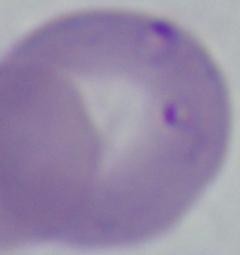

magnification = 1000x
modality = micrograph
identification = Babesia